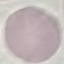

result: no malaria parasites detected
capture: smartphone through the microscope eyepiece
stain: Giemsa
preparation: thin blood film
image_type: automatically extracted cell patch, resized to 64 × 64 pixels